Assess this cell for malaria.
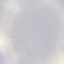
It is uninfected.

Summary:
  - Preparation: thin blood film
  - Stain: Giemsa
  - Image type: automatically extracted cell patch, resized to 64 × 64 pixels
  - Capture: smartphone camera at the microscope eyepiece